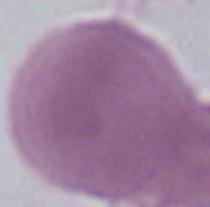
Summary:
  - Identification: red blood cell
  - Modality: micrograph
  - Magnification: 1000x